Report the malaria status of this cell.
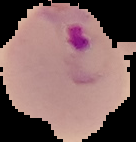

Parasitized.

{
  "preparation": "thin blood smear",
  "image_type": "segmented cell region with the area outside set to black",
  "image_size": "136×142 pixels"
}